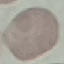
Summary:
  - Malaria status: uninfected
  - Preparation: thin blood smear
  - Image type: automatically extracted cell patch, resized to 64 × 64 pixels
  - Stain: Giemsa
  - Capture: smartphone through the microscope eyepiece